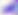
{
  "modality": "micrograph",
  "identification": "Toxoplasma gondii",
  "magnification": "400x"
}